State the blood parasite species.
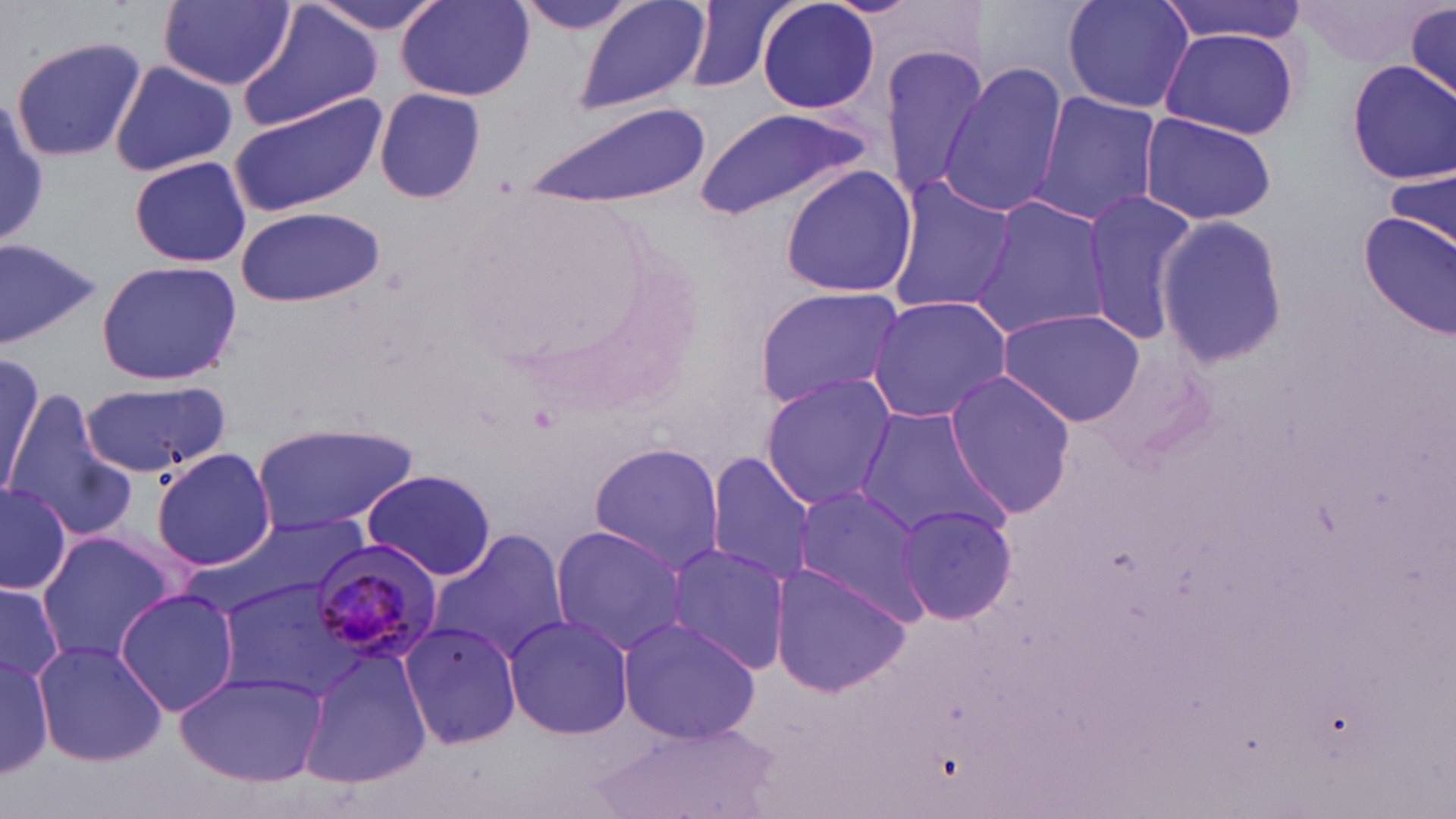

Plasmodium malariae.

Summary:
  - Coordinate format: approximate bounding boxes as (x1, y1, x2, y2) in pixels
  - Plasmodium malariae-infected red blood cell locations: (305, 542, 442, 665)
  - Uninfected red blood cell locations: (307, 0, 448, 37), (508, 0, 649, 35), (573, 0, 713, 117), (756, 0, 881, 115), (1061, 0, 1194, 114), (1156, 0, 1309, 46), (1401, 0, 1456, 100), (159, 1, 295, 90), (683, 1, 798, 94), (397, 2, 532, 102), (236, 6, 382, 133), (1159, 26, 1300, 141), (10, 35, 148, 164), (877, 43, 990, 203), (110, 60, 237, 176), (1348, 61, 1455, 182), (938, 64, 1066, 217), (374, 88, 485, 204), (1032, 92, 1162, 225), (228, 95, 385, 216), (522, 100, 712, 208), (693, 106, 874, 221), (1139, 113, 1278, 226), (127, 154, 256, 268), (778, 164, 918, 299), (1384, 165, 1456, 259), (883, 176, 1018, 318), (1081, 190, 1201, 345), (975, 195, 1110, 337), (235, 205, 386, 308), (1360, 211, 1456, 342), (1154, 213, 1287, 369), (0, 237, 103, 350), (96, 260, 242, 386), (752, 285, 907, 413), (865, 295, 1014, 425), (994, 308, 1147, 426), (0, 351, 45, 496), (943, 369, 1078, 516), (759, 375, 897, 509), (82, 380, 229, 480), (6, 399, 137, 541), (852, 406, 1009, 542), (251, 420, 420, 536), (588, 442, 727, 572), (153, 447, 275, 571), (703, 455, 817, 587), (361, 467, 498, 581), (0, 480, 72, 596), (791, 485, 934, 622), (897, 503, 1019, 628), (183, 511, 382, 624), (547, 525, 687, 657), (430, 531, 571, 666), (36, 532, 181, 664), (663, 543, 793, 676), (767, 563, 912, 700), (213, 577, 368, 701), (0, 579, 65, 689), (116, 587, 239, 717), (503, 612, 635, 742), (617, 616, 762, 745), (399, 620, 523, 751), (32, 638, 167, 768), (297, 644, 433, 791), (0, 645, 56, 779), (175, 668, 329, 786), (594, 722, 778, 819)
  - Modality: light microscopy
  - Magnification: 1000x
  - Image size: 1456×819 pixels
  - Preparation: thin blood smear
  - Stain: May-Grünwald-Giemsa
  - Field of view: one of a larger specimen